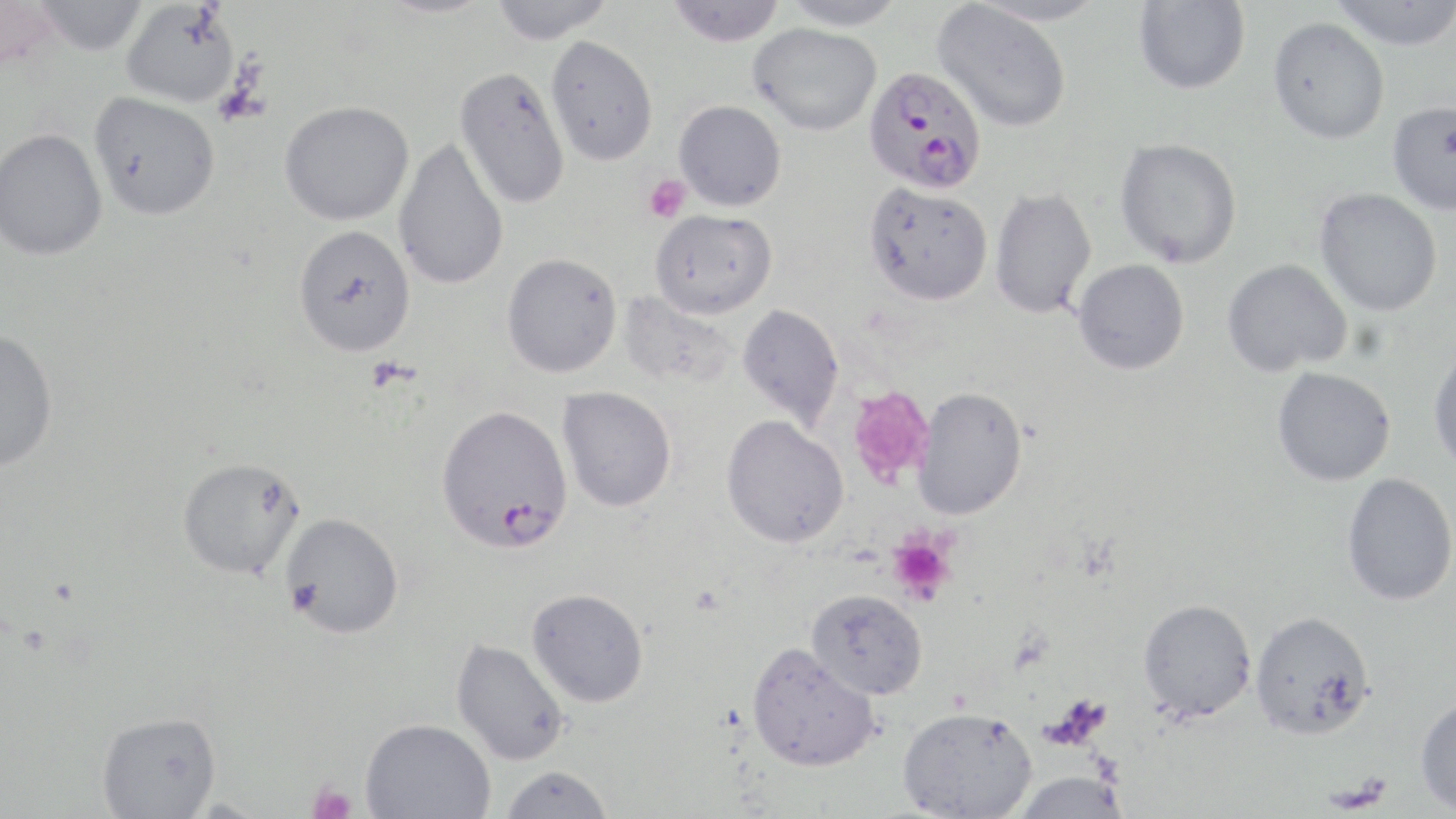

Approximate bounding boxes as named x1/y1/x2/y2 corners in pixels. Platelet locations: (x1=643, y1=174, x2=690, y2=223), (x1=848, y1=386, x2=935, y2=486), (x1=885, y1=531, x2=956, y2=605), (x1=306, y1=780, x2=358, y2=819). Plasmodium falciparum-infected red blood cell locations: (x1=863, y1=66, x2=986, y2=193), (x1=436, y1=404, x2=573, y2=554). Uninfected red blood cell locations: (x1=32, y1=0, x2=148, y2=56), (x1=375, y1=0, x2=497, y2=18), (x1=489, y1=0, x2=613, y2=44), (x1=667, y1=0, x2=786, y2=47), (x1=780, y1=0, x2=906, y2=30), (x1=1133, y1=0, x2=1250, y2=94), (x1=1329, y1=0, x2=1456, y2=50), (x1=0, y1=1, x2=57, y2=75), (x1=121, y1=2, x2=240, y2=108), (x1=933, y1=2, x2=1072, y2=132), (x1=1267, y1=17, x2=1390, y2=144), (x1=748, y1=22, x2=881, y2=136), (x1=546, y1=36, x2=658, y2=166), (x1=455, y1=66, x2=570, y2=210), (x1=89, y1=92, x2=221, y2=220), (x1=673, y1=100, x2=787, y2=211), (x1=1386, y1=100, x2=1456, y2=216), (x1=279, y1=101, x2=414, y2=226), (x1=0, y1=128, x2=107, y2=261), (x1=393, y1=138, x2=510, y2=291), (x1=1115, y1=138, x2=1242, y2=268), (x1=864, y1=182, x2=993, y2=305), (x1=1315, y1=187, x2=1443, y2=316), (x1=989, y1=188, x2=1097, y2=319), (x1=650, y1=209, x2=778, y2=318), (x1=292, y1=224, x2=415, y2=357), (x1=501, y1=253, x2=622, y2=377), (x1=1072, y1=259, x2=1190, y2=375), (x1=1222, y1=259, x2=1351, y2=377), (x1=737, y1=303, x2=845, y2=430), (x1=0, y1=329, x2=58, y2=472), (x1=1428, y1=345, x2=1456, y2=476), (x1=1272, y1=366, x2=1396, y2=486), (x1=557, y1=386, x2=677, y2=512), (x1=912, y1=386, x2=1028, y2=519), (x1=721, y1=415, x2=849, y2=548), (x1=176, y1=457, x2=306, y2=580), (x1=1341, y1=473, x2=1456, y2=606), (x1=279, y1=512, x2=404, y2=639), (x1=526, y1=587, x2=649, y2=707), (x1=806, y1=589, x2=927, y2=699), (x1=1138, y1=598, x2=1257, y2=721), (x1=1250, y1=611, x2=1376, y2=740), (x1=451, y1=638, x2=571, y2=765), (x1=747, y1=642, x2=880, y2=772), (x1=1414, y1=695, x2=1456, y2=815), (x1=898, y1=706, x2=1037, y2=818), (x1=95, y1=711, x2=221, y2=818), (x1=361, y1=717, x2=496, y2=818), (x1=499, y1=764, x2=614, y2=818), (x1=1010, y1=770, x2=1131, y2=818). Slide-level diagnosis: Plasmodium falciparum. Optical microscopy. Image is 1456×819 pixels. May-Grünwald-Giemsa-stained preparation. Thin blood film. One field of a larger specimen. Captured at 1000x magnification.